Name the cell type shown.
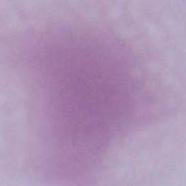
This is an erythrocyte.

magnification = 1000x
modality = photomicrograph